Assess the morphology of the red blood cells.
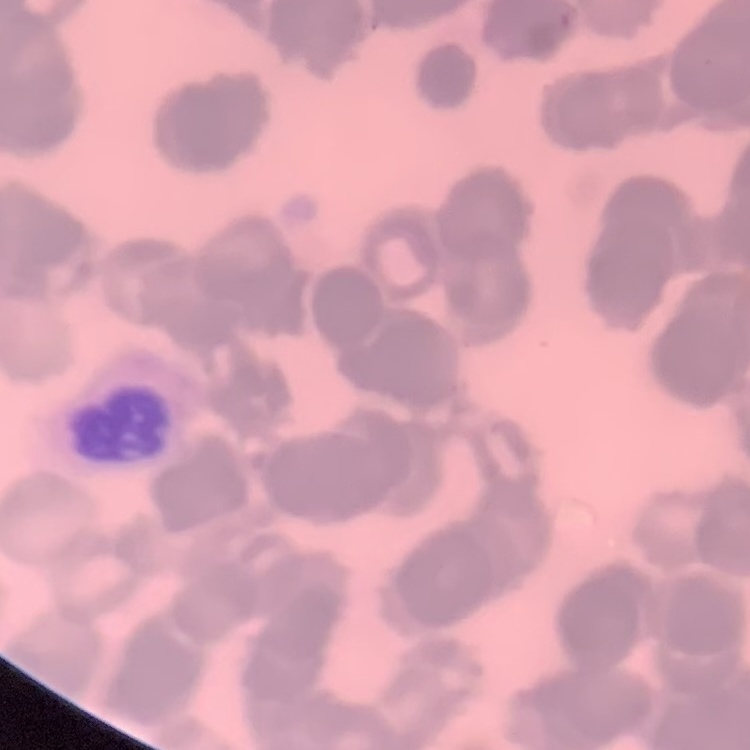

They show rouleaux formation.

Summary:
  - Preparation: thin blood film
  - Stain: Field's or Giemsa
  - Image type: one tile cut from a larger photomicrograph